Report the malaria status of this cell.
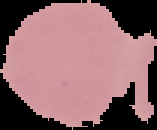

Uninfected.

Summary:
  - Preparation: thin blood film
  - Image size: 157×130 pixels
  - Image type: cell region segmented out of the field of view; surrounding area masked to black